Point out cells.
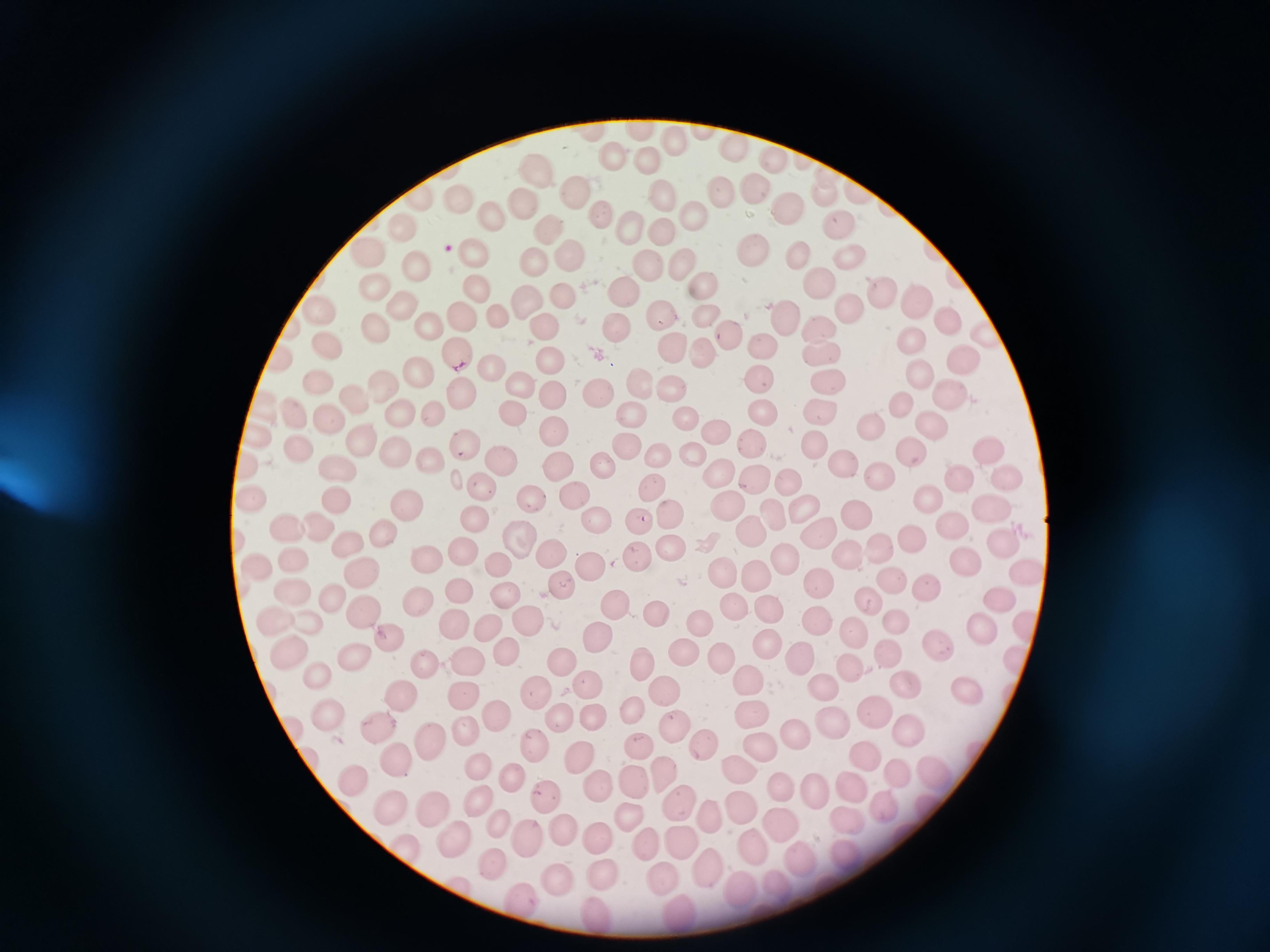

Approximate centers as (x, y) in pixels.
Cells: (641, 130), (673, 142), (736, 146), (613, 155), (775, 159), (646, 164), (533, 172), (750, 188), (577, 193), (663, 193), (726, 193), (825, 193), (422, 197), (462, 202), (786, 206), (520, 208), (695, 210), (492, 215), (596, 216), (839, 220), (401, 224), (633, 225), (547, 227), (662, 231), (751, 245), (365, 250), (850, 253), (798, 254), (473, 255), (568, 256), (530, 260), (681, 262), (416, 265), (649, 267), (817, 280), (704, 285), (375, 286), (624, 288), (477, 289), (878, 290), (562, 296), (528, 298), (913, 298), (404, 308), (849, 308), (322, 310), (663, 312), (462, 315), (702, 315), (497, 316), (785, 316), (946, 316), (540, 324), (426, 325), (620, 325), (377, 326), (818, 326), (726, 337), (915, 338), (761, 341), (329, 345), (671, 346), (700, 352), (459, 354), (823, 355), (550, 356), (962, 357), (285, 359), (492, 367), (418, 371), (916, 373), (829, 377), (758, 379), (318, 380), (385, 382), (520, 382), (637, 382), (671, 389), (598, 390), (461, 393), (949, 393), (553, 395), (355, 400), (904, 403), (262, 405), (632, 408), (291, 409), (763, 411), (819, 411), (401, 412), (434, 413), (511, 414), (686, 416), (328, 420), (870, 424), (934, 424), (558, 428), (719, 429), (257, 436), (362, 440), (628, 442), (750, 442), (815, 443), (463, 444), (300, 446), (908, 448), (984, 449), (658, 452), (394, 453), (691, 453), (500, 457), (428, 460), (560, 462), (844, 464), (248, 466), (605, 467), (337, 469), (718, 469), (879, 476), (750, 477), (1000, 477), (960, 481), (651, 483), (789, 483), (480, 484), (532, 492), (928, 496), (253, 497), (574, 497), (338, 500), (405, 503), (987, 506), (728, 508), (801, 509), (772, 513), (855, 513), (669, 516), (473, 518), (598, 520), (641, 522), (953, 525), (322, 527), (292, 529), (382, 530), (814, 533), (751, 534), (915, 535), (522, 539), (1002, 539), (347, 541), (670, 546), (465, 549), (883, 550), (844, 551), (551, 553), (637, 553), (295, 558), (965, 560), (260, 561), (427, 561), (781, 561), (496, 563), (590, 564), (361, 571), (1022, 573), (720, 574), (756, 575), (892, 580), (816, 583), (560, 585), (927, 588), (458, 592), (294, 593), (331, 597), (503, 597), (415, 598), (1001, 599), (868, 601), (736, 607), (616, 608), (772, 609), (366, 611), (656, 612), (276, 614), (454, 616), (820, 618), (310, 621), (895, 621), (528, 622), (981, 625), (699, 626), (488, 627), (1027, 627), (854, 630), (391, 636), (598, 637), (939, 646), (764, 647), (504, 650), (889, 650), (681, 653), (356, 657), (721, 657), (800, 657), (1018, 657), (287, 658), (464, 660), (565, 662), (425, 663), (643, 663), (850, 669), (317, 677), (749, 679), (905, 683), (589, 684), (818, 686), (664, 687), (538, 689), (969, 689), (466, 692), (407, 693), (873, 712), (493, 713), (634, 713), (329, 714), (562, 714), (592, 714), (752, 716), (829, 720), (382, 722), (673, 722), (910, 727), (295, 729), (465, 732), (796, 734), (428, 739), (699, 741), (541, 742), (640, 745), (764, 748), (580, 754), (864, 755), (395, 756), (930, 768), (479, 769), (662, 769), (737, 770), (897, 771), (354, 776), (511, 778), (636, 782), (595, 783), (782, 784), (854, 786), (816, 789), (542, 793), (681, 801), (480, 804), (887, 804), (741, 805), (393, 808), (434, 812), (629, 813), (845, 814), (708, 815), (502, 823), (779, 823), (559, 826), (451, 835), (683, 836), (595, 839), (528, 840), (646, 842), (751, 844), (402, 848), (800, 860), (704, 863), (491, 864), (604, 873), (662, 876), (561, 879), (783, 886), (743, 888), (521, 904), (679, 913), (594, 914).

Summary:
  - Stain: Giemsa
  - Preparation: thin smear
  - Capture: smartphone through the microscope eyepiece
  - Image size: 1270×952 pixels
  - Field of view: single